Identify the parasite.
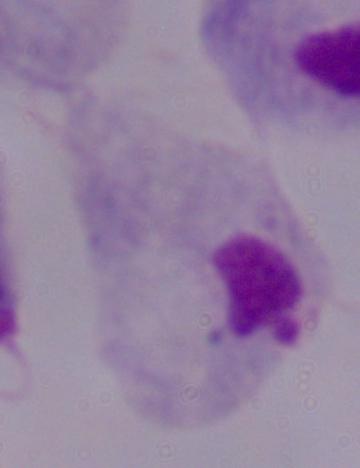

This is a trichomonad.

Summary:
  - Magnification: 1000x
  - Modality: micrograph